Locate every blood parasite and identify its species.
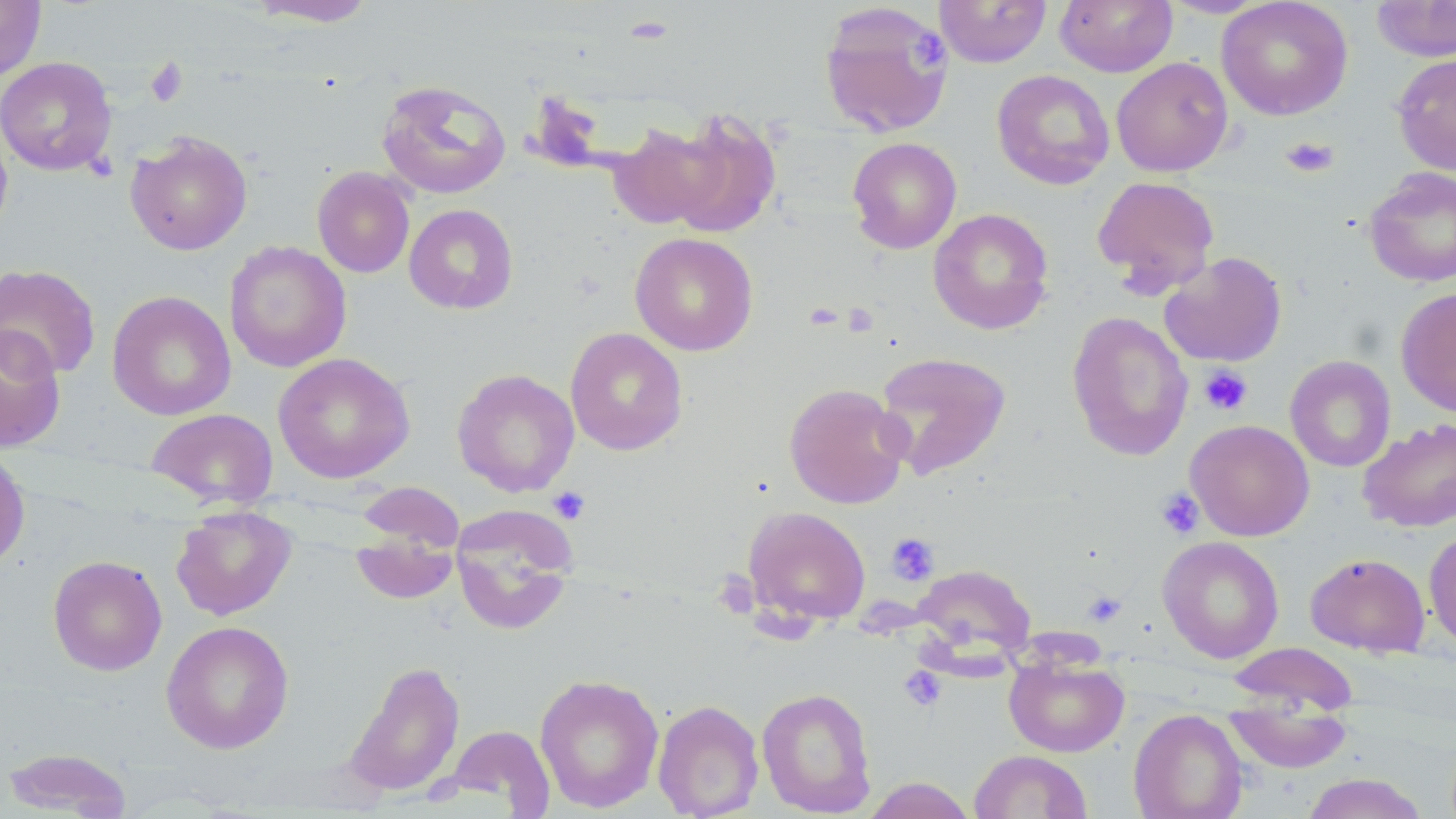
No blood parasites seen.

Approximate bounding boxes as (x1, y1, x2, y2) in pixels. Platelet locations: (909, 33, 949, 71), (145, 58, 188, 107), (1281, 136, 1339, 178), (843, 302, 879, 337), (1199, 365, 1253, 416), (548, 486, 590, 524), (1156, 487, 1205, 539), (886, 532, 939, 584), (711, 571, 760, 619), (1083, 591, 1126, 627), (899, 666, 946, 712). Uninfected red blood cell locations: (0, 0, 46, 81), (246, 0, 379, 27), (934, 0, 1052, 67), (1055, 0, 1178, 77), (1159, 0, 1272, 18), (1217, 0, 1353, 120), (1371, 0, 1456, 62), (818, 2, 954, 138), (1391, 53, 1456, 175), (1112, 56, 1233, 177), (0, 57, 117, 176), (992, 69, 1114, 189), (376, 79, 511, 199), (662, 110, 782, 239), (0, 119, 13, 241), (609, 121, 726, 231), (125, 131, 252, 255), (847, 137, 961, 254), (312, 166, 415, 278), (1364, 167, 1456, 287), (1091, 175, 1220, 294), (404, 204, 518, 314), (928, 208, 1054, 335), (630, 232, 759, 356), (224, 240, 351, 372), (1159, 251, 1287, 367), (0, 263, 101, 380), (1395, 287, 1456, 416), (107, 290, 236, 421), (1066, 311, 1194, 461), (0, 325, 66, 453), (565, 327, 688, 456), (874, 351, 1012, 480), (273, 352, 416, 483), (1285, 355, 1396, 472), (452, 368, 580, 496), (784, 382, 910, 509), (146, 407, 279, 509), (1358, 418, 1456, 532), (1185, 419, 1314, 541), (0, 447, 30, 570), (355, 481, 465, 553), (450, 505, 579, 636), (171, 506, 298, 621), (742, 506, 871, 626), (1423, 529, 1456, 651), (350, 533, 460, 604), (1158, 536, 1284, 663), (1305, 553, 1430, 657), (47, 555, 166, 675), (913, 563, 1036, 665), (161, 620, 294, 754), (1226, 642, 1359, 716), (1004, 654, 1129, 757), (344, 660, 465, 798), (534, 672, 665, 813), (757, 686, 877, 816), (653, 699, 765, 818), (1224, 699, 1354, 774), (1128, 708, 1248, 819), (446, 725, 554, 813), (3, 747, 133, 818), (969, 750, 1093, 819), (1301, 772, 1428, 819), (861, 777, 978, 819). Slide-level diagnosis: no evidence of blood parasites. Image is 1456×819 pixels. Thin blood smear. Light microscopy. May-Grünwald-Giemsa-stained preparation. Single field of view. Captured at 1000x magnification.